Assess this cell for malaria.
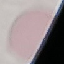

It is uninfected.

Cell patch, automatically extracted from a larger field of view and resized to 64 × 64 pixels. Photographed with a smartphone camera at the microscope eyepiece. Giemsa stain. Thin blood smear.